Comment on the morphology of the erythrocytes.
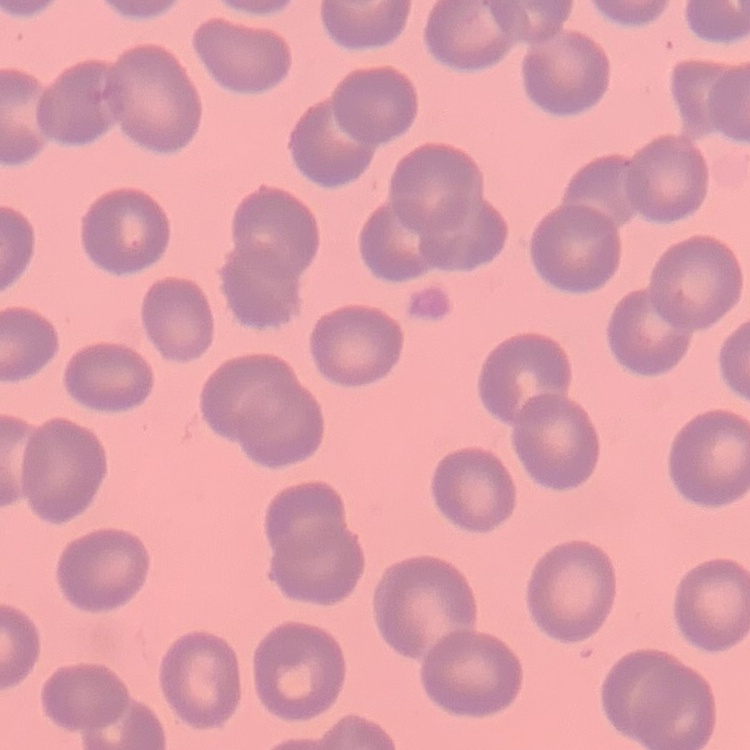
No rouleaux formation.

stain = Field's or Giemsa
image type = square crop of a larger photomicrograph
preparation = thin blood smear